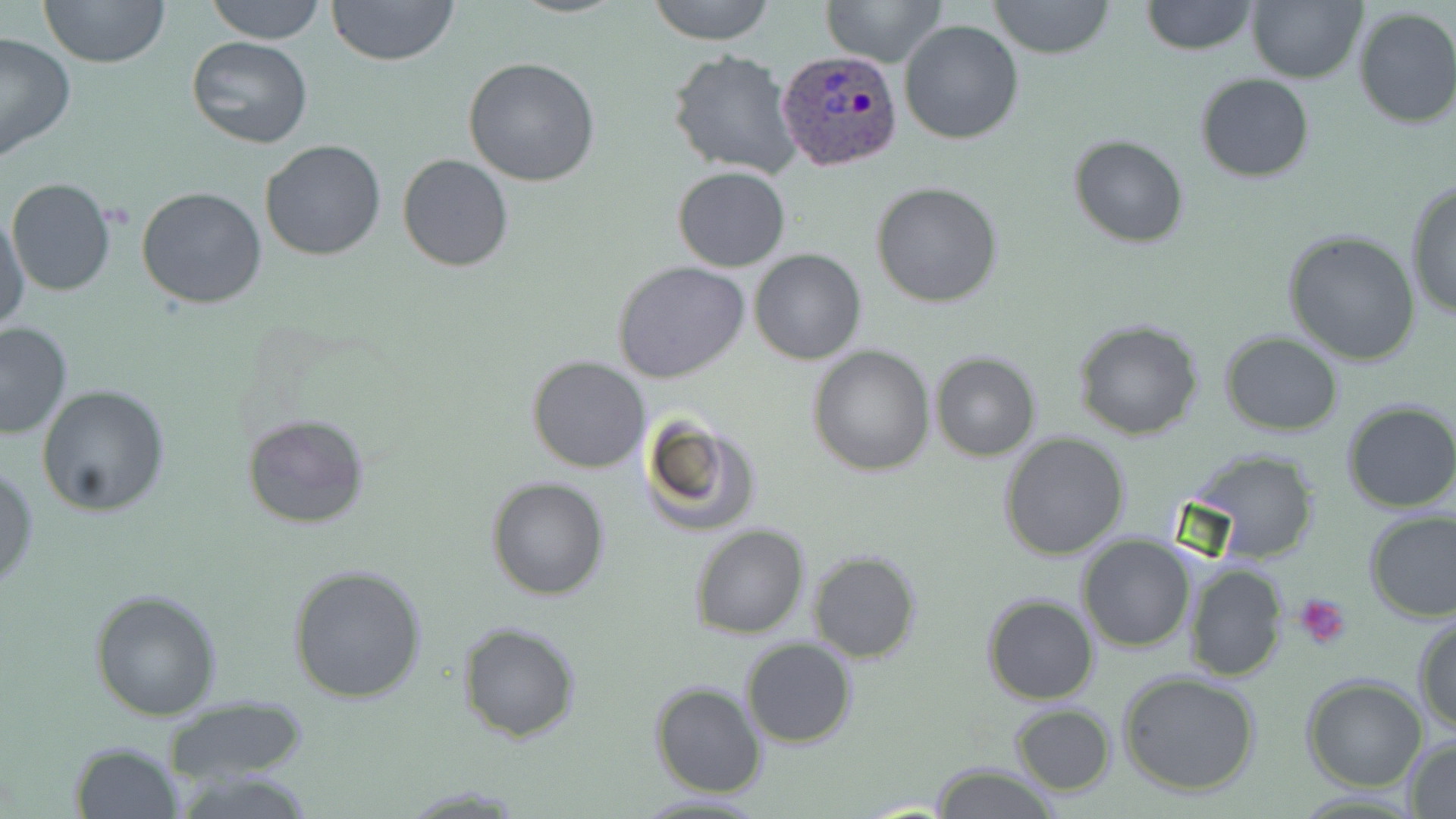

Summary:
  - Coordinate format: approximate bounding boxes as [x1, y1, x2, y2] in pixels
  - Platelet locations: [1294, 593, 1353, 650]
  - Uninfected red blood cell locations: [38, 0, 170, 69], [204, 0, 327, 44], [326, 0, 460, 68], [645, 0, 777, 45], [823, 0, 945, 68], [987, 0, 1115, 58], [1246, 0, 1365, 84], [1142, 1, 1257, 55], [1351, 6, 1456, 129], [897, 19, 1025, 144], [0, 31, 75, 163], [185, 37, 314, 151], [667, 50, 802, 179], [462, 57, 600, 187], [1195, 74, 1316, 183], [1068, 135, 1188, 247], [261, 138, 385, 260], [398, 153, 515, 272], [672, 167, 790, 272], [7, 178, 116, 296], [871, 181, 1004, 307], [1404, 181, 1456, 324], [137, 186, 267, 309], [1, 212, 30, 328], [1282, 229, 1423, 366], [750, 249, 866, 365], [612, 261, 751, 384], [1072, 317, 1205, 440], [0, 321, 73, 441], [1219, 331, 1344, 436], [807, 346, 935, 476], [930, 352, 1042, 460], [527, 356, 650, 474], [37, 385, 170, 518], [1341, 401, 1456, 514], [242, 413, 369, 530], [637, 413, 760, 539], [999, 433, 1130, 559], [1191, 451, 1323, 564], [0, 464, 39, 591], [486, 476, 611, 600], [1363, 508, 1456, 623], [688, 525, 811, 640], [1078, 536, 1197, 654], [807, 551, 922, 662], [1181, 560, 1288, 682], [286, 563, 428, 705], [89, 588, 223, 720], [981, 594, 1099, 705], [1413, 615, 1456, 735], [457, 621, 581, 742], [741, 639, 855, 749], [1117, 670, 1262, 796], [1302, 676, 1428, 791], [650, 680, 767, 798], [164, 696, 307, 785], [1010, 703, 1116, 795], [1402, 735, 1456, 817], [70, 741, 184, 819], [931, 763, 1058, 819], [629, 791, 770, 818]
  - Plasmodium ovale-infected red blood cell locations: [776, 50, 904, 173]
  - Slide-level diagnosis: Plasmodium ovale
  - Magnification: 1000x
  - Preparation: thin blood smear
  - Modality: optical microscopy
  - Stain: May-Grünwald-Giemsa
  - Field of view: one of a larger specimen
  - Image size: 1456×819 pixels